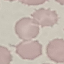
Summary:
  - Malaria status: uninfected
  - Stain: Giemsa
  - Image type: automatically extracted cell patch, resized to 64 × 64 pixels
  - Preparation: thin blood film
  - Capture: smartphone camera at the microscope eyepiece